Identify the preparation type.
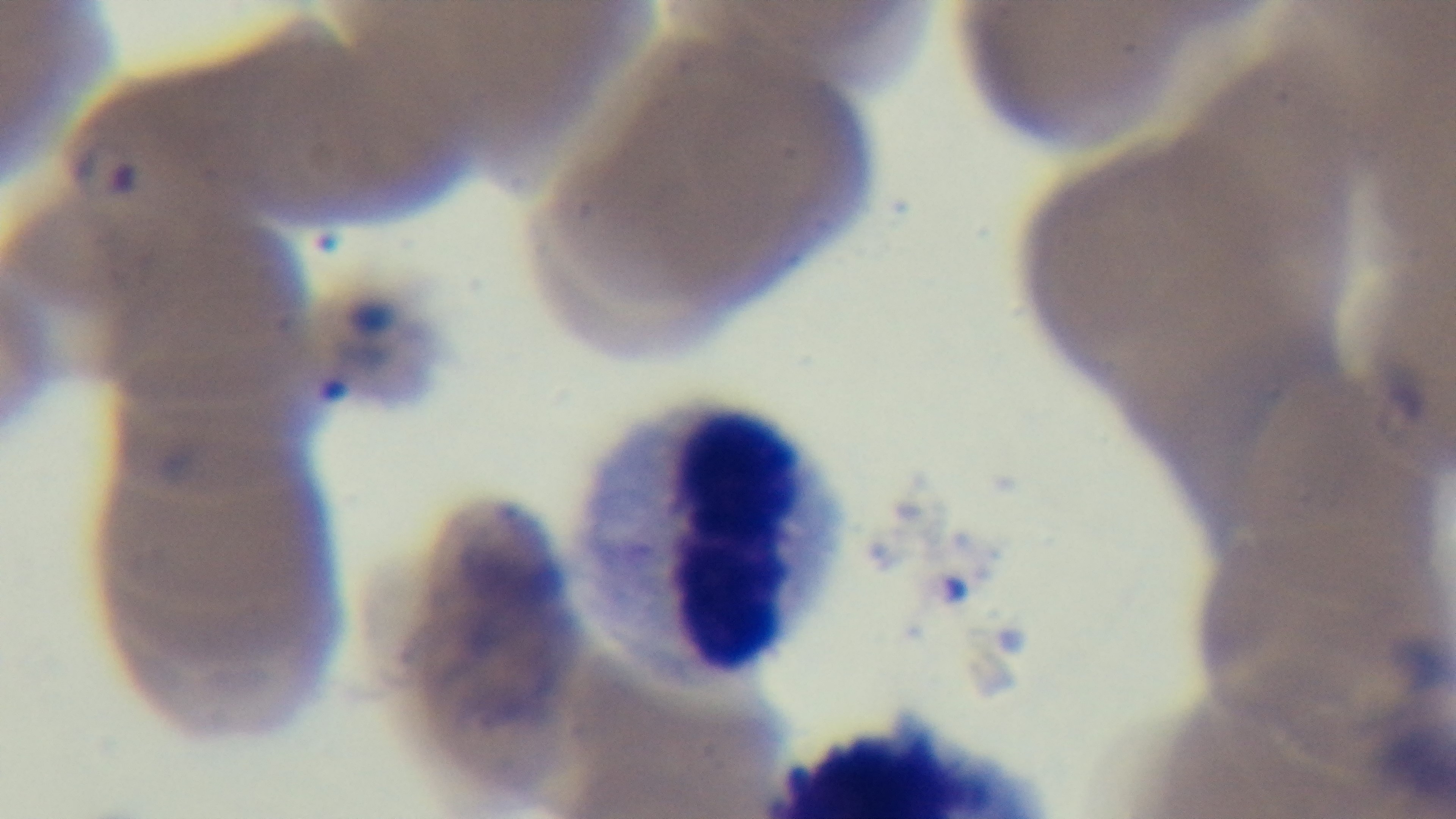
A thin smear.

Summary:
  - Stain: Giemsa
  - Modality: light microscopy
  - Objective: 100x oil immersion
  - Field of view: one from the slide
  - Malaria status: positive
  - Capture: mounted 4K digital camera